Give the preparation type.
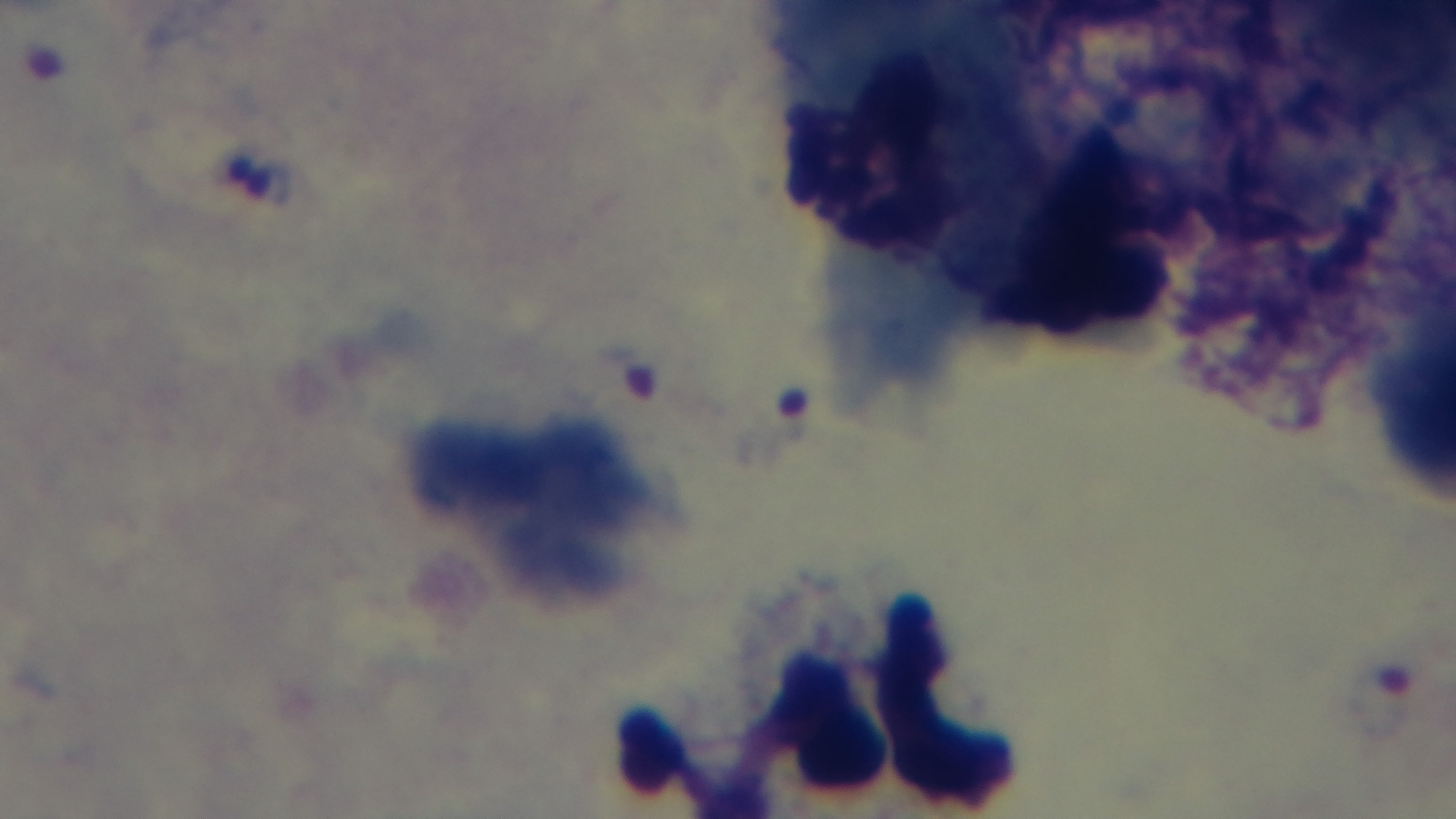

It is a thick blood film.

Giemsa stain. Single field of view. Malaria status: infected. Captured with a mounted 4K digital camera. Oil-immersion objective, 100x. Light microscopy.